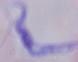
1000x magnification. Photomicrograph. A trypanosome is seen.